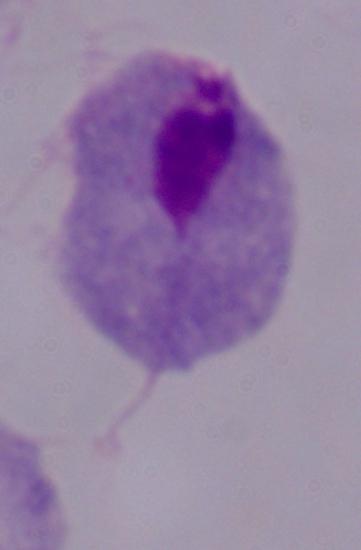
Summary:
  - Magnification: 1000x
  - Modality: micrograph
  - Identification: trichomonad